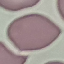
malaria status = uninfected
stain = Giemsa
image type = automatically extracted cell patch, resized to 64 × 64 pixels
preparation = thin blood smear
capture = smartphone camera at the microscope eyepiece